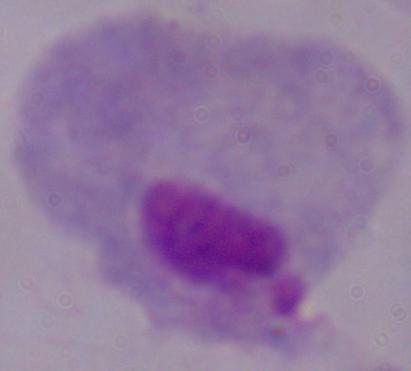
Summary:
  - Identification: trichomonad
  - Magnification: 1000x
  - Modality: micrograph